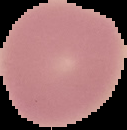

Summary:
  - Preparation: thin blood smear
  - Malaria status: uninfected
  - Image type: segmented cell region with the area outside set to black
  - Image size: 127×130 pixels